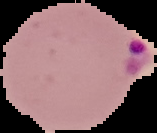
result = Plasmodium parasites detected
image type = segmented cell region on a black background
image size = 157×133 pixels
preparation = thin blood smear